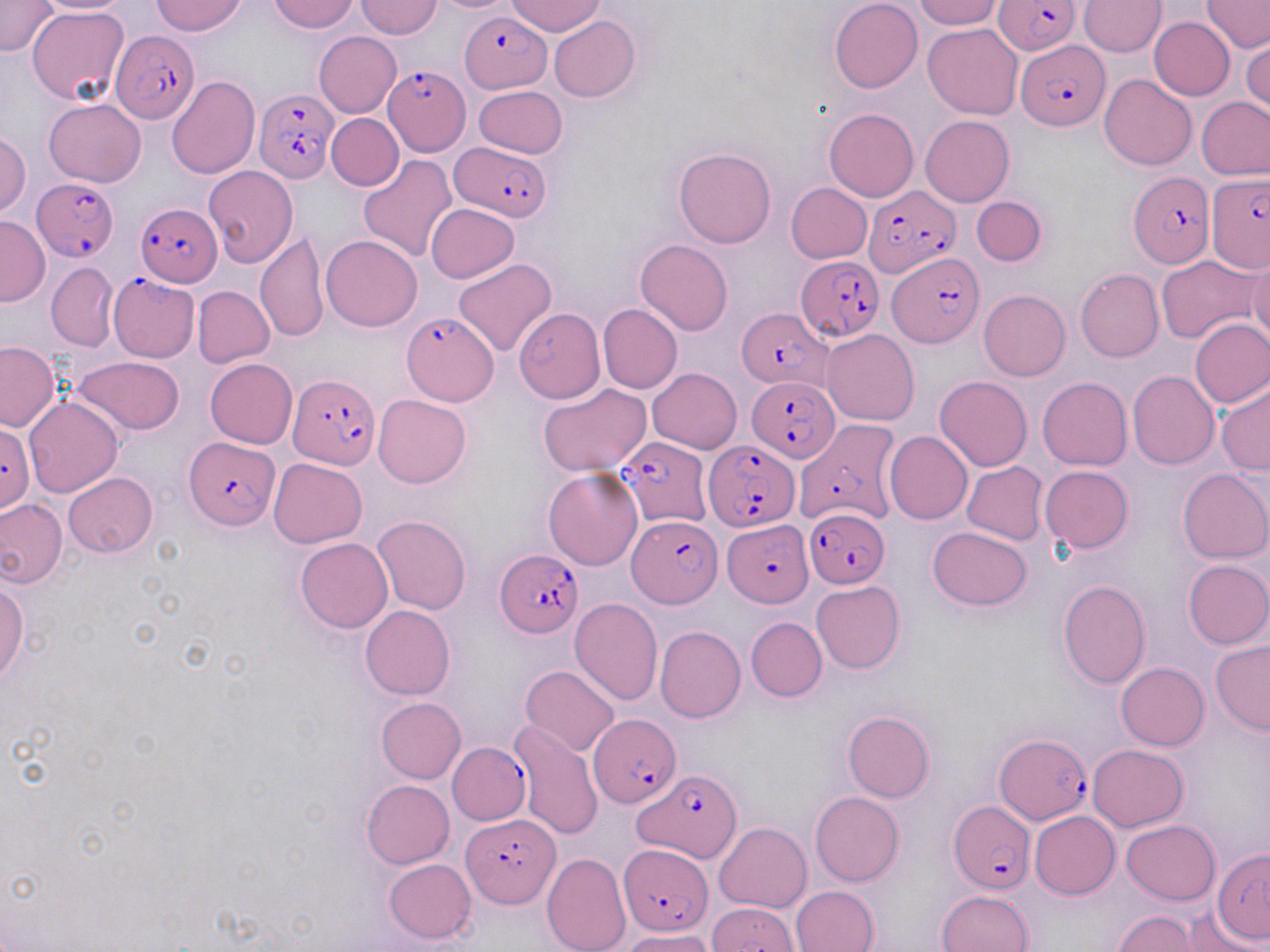
{
  "slide_level_diagnosis": "Plasmodium falciparum",
  "image_size": "1270×952 pixels",
  "uninfected_red_blood_cell_locations": "approximate bounding boxes as (x1,y1)-(x2,y2) corner pairs in pixels: (32,0)-(138,14), (151,0)-(248,36), (270,0)-(359,33), (506,0)-(606,37), (830,0)-(923,92), (914,0)-(1004,29), (1080,0)-(1165,56), (1202,0)-(1269,54), (355,1)-(443,39), (0,2)-(59,56), (27,7)-(129,107), (548,16)-(640,103), (1149,17)-(1236,101), (922,23)-(1023,119), (314,32)-(401,117), (1242,37)-(1269,116), (1099,73)-(1197,170), (167,77)-(260,181), (472,85)-(567,159), (1196,96)-(1270,180), (44,98)-(146,187), (823,108)-(919,201), (326,113)-(403,191), (921,115)-(1014,207), (0,132)-(31,218), (673,147)-(776,249), (357,155)-(458,264), (202,166)-(298,268), (786,182)-(872,263), (973,196)-(1047,266), (425,204)-(520,283), (0,215)-(49,306), (255,234)-(329,342), (321,235)-(422,331), (635,239)-(732,335), (1247,253)-(1270,344), (1156,255)-(1260,343), (453,258)-(556,357), (46,263)-(119,351), (1075,268)-(1163,362), (193,286)-(274,367), (979,290)-(1069,381), (598,303)-(682,393), (513,308)-(605,403), (1189,317)-(1270,409), (821,330)-(920,425), (0,341)-(59,431), (72,354)-(185,435), (204,359)-(297,449), (647,368)-(741,453), (1128,370)-(1219,470), (934,376)-(1031,471), (1038,377)-(1132,470), (1216,382)-(1270,475), (538,383)-(652,475), (372,394)-(471,488), (23,397)-(122,499), (884,431)-(972,526), (268,458)-(367,548), (962,461)-(1048,546), (1041,465)-(1133,553), (544,468)-(643,570), (1177,469)-(1270,564), (63,471)-(158,558), (0,497)-(66,589), (372,515)-(472,614), (927,526)-(1032,609), (296,537)-(393,633), (1182,559)-(1270,649), (0,577)-(28,682), (1057,580)-(1150,688), (812,581)-(905,674), (569,599)-(663,706), (361,605)-(455,700), (746,617)-(827,702), (656,626)-(746,722), (1209,641)-(1270,735), (1116,662)-(1209,750), (520,665)-(620,756), (377,697)-(466,783), (842,711)-(934,802), (510,720)-(604,840), (1088,744)-(1188,832), (362,779)-(455,868), (810,791)-(904,886), (1030,810)-(1120,899), (1121,819)-(1220,904), (714,822)-(812,913), (1212,848)-(1270,946), (541,851)-(631,952), (384,858)-(476,944), (791,885)-(878,952), (936,889)-(1034,952), (706,903)-(800,952), (1113,910)-(1200,951), (1177,910)-(1261,952), (623,929)-(717,952)",
  "field_of_view": "single",
  "magnification": "1000x",
  "modality": "light microscopy",
  "stain": "May-Grünwald-Giemsa",
  "preparation": "thin blood film",
  "plasmodium_falciparum_infected_red_blood_cell_locations": "approximate bounding boxes as (x1,y1)-(x2,y2) corner pairs in pixels: (994,0)-(1081,54), (459,12)-(551,93), (111,33)-(200,127), (1018,41)-(1109,130), (382,66)-(471,156), (254,88)-(337,183), (452,144)-(549,218), (1128,171)-(1214,268), (1205,172)-(1269,273), (31,177)-(121,262), (862,185)-(959,277), (137,201)-(222,287), (887,253)-(985,347), (795,256)-(883,341), (107,274)-(200,362), (737,309)-(832,391), (403,312)-(496,405), (287,374)-(378,472), (746,375)-(840,461), (794,418)-(901,528), (0,425)-(35,512), (616,436)-(711,528), (184,437)-(279,531), (704,440)-(796,532), (804,508)-(889,586), (627,514)-(719,607), (723,519)-(813,606), (495,548)-(584,637), (588,713)-(680,805), (994,732)-(1093,825), (447,743)-(529,825), (636,769)-(741,863), (947,801)-(1036,896), (461,814)-(558,908), (621,846)-(711,935)"
}